Describe the morphology of the red blood cells.
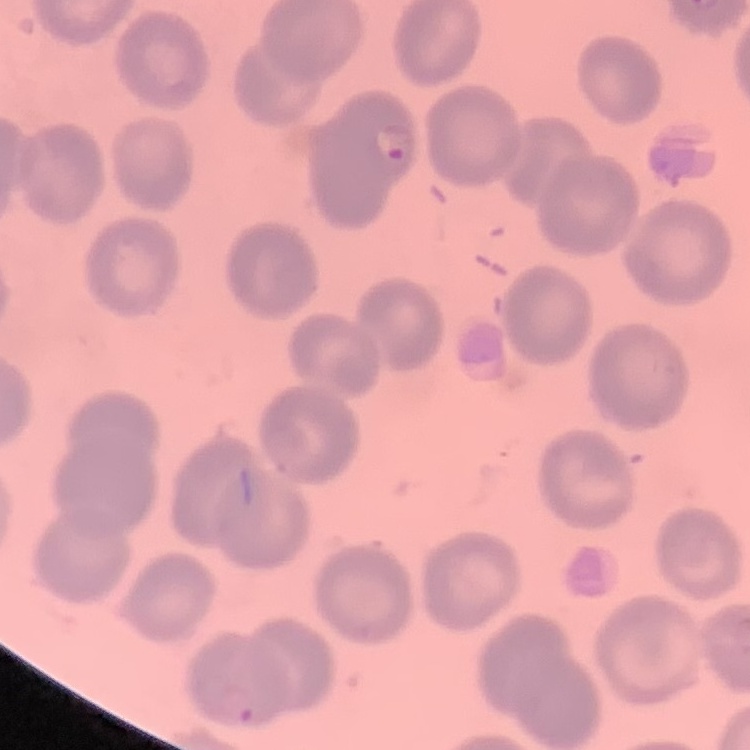

No rouleaux formation.

{
  "preparation": "thin blood film",
  "image_type": "one tile cut from a larger photomicrograph",
  "stain": "Field's or Giemsa"
}